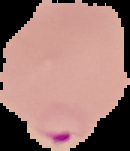

{
  "preparation": "thin blood smear",
  "image_size": "130×151 pixels",
  "image_type": "segmented cell region on a black background",
  "result": "Plasmodium parasites identified"
}